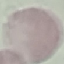
Summary:
  - Result: negative for malaria parasites
  - Stain: Giemsa
  - Capture: smartphone through the microscope eyepiece
  - Preparation: thin blood smear
  - Image type: cell patch, automatically extracted from a larger field of view and resized to 64 × 64 pixels